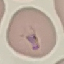

Summary:
  - Result: malaria parasites detected
  - Image type: automatically extracted cell patch, resized to 64 × 64 pixels
  - Preparation: thin smear
  - Stain: Giemsa
  - Capture: smartphone through the microscope eyepiece